Evaluate for Plasmodium parasites.
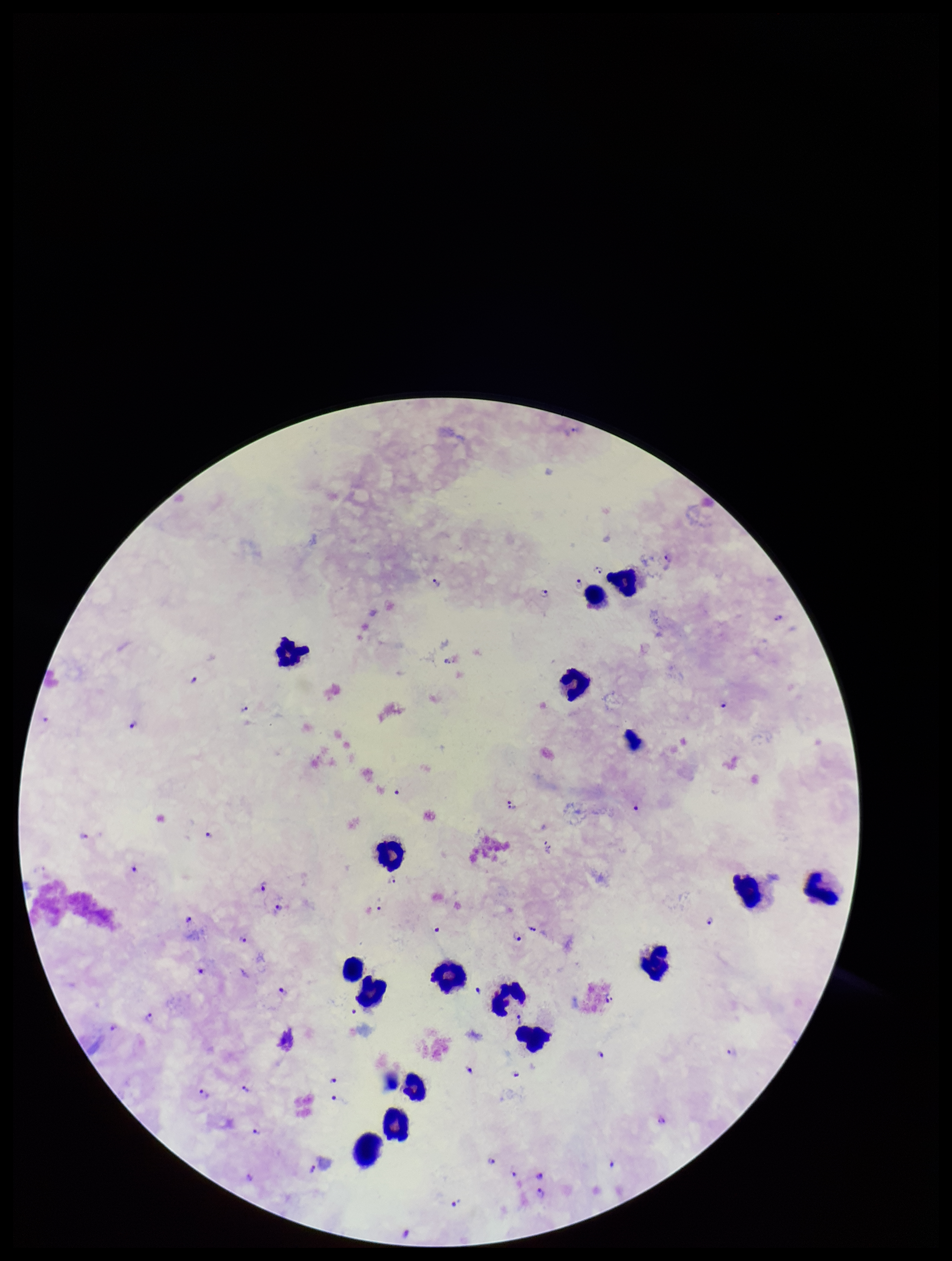
Seen.

Summary:
  - Stain: Giemsa
  - Parasite count: 54
  - Patient malaria status: positive
  - Field of view: single
  - Leukocyte count: 17
  - Capture: smartphone photograph through the microscope eyepiece
  - Preparation: thick blood smear
  - Image size: 952×1261 pixels
  - Species reported for this patient: Plasmodium falciparum